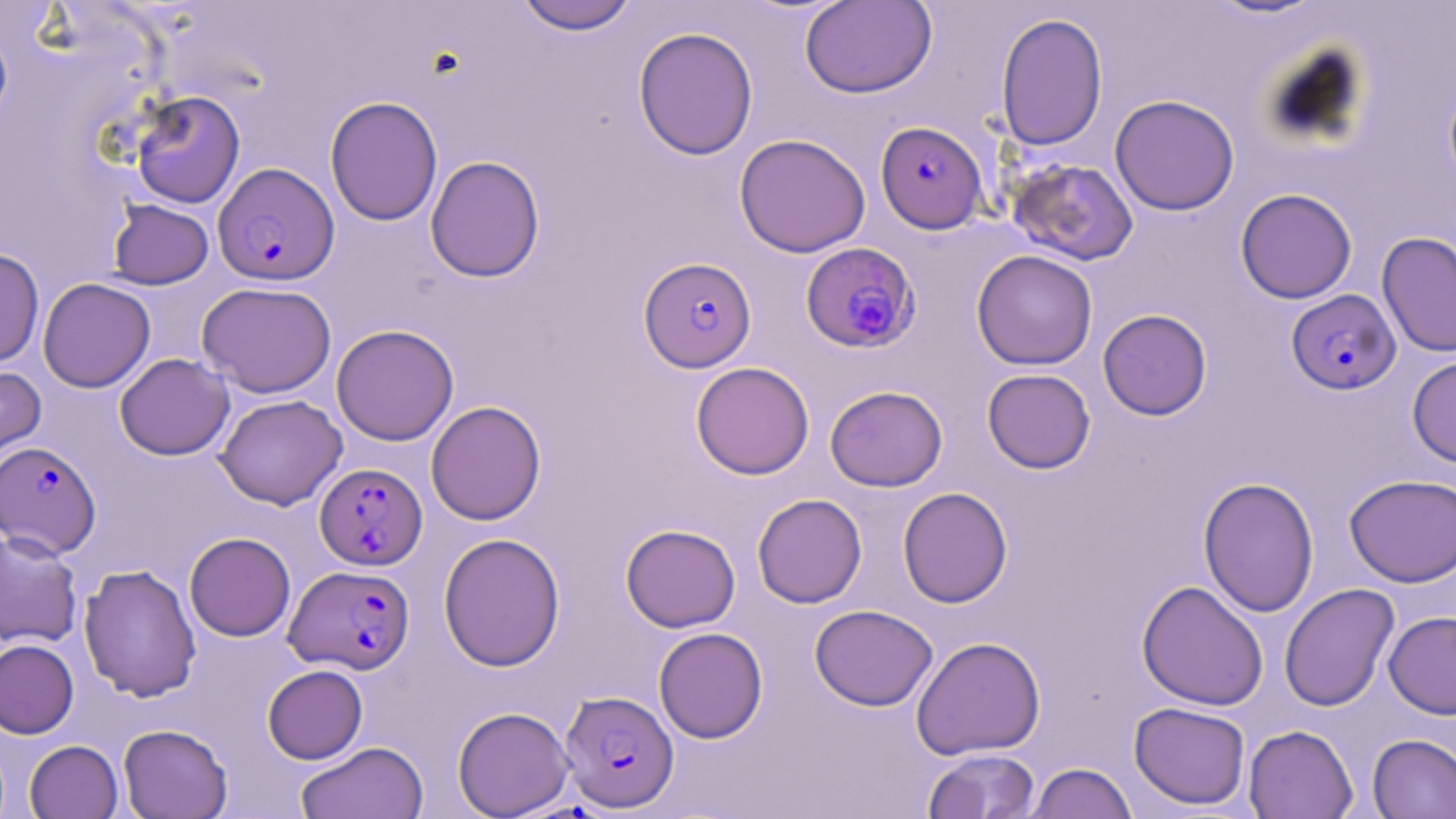
Summary:
  - Coordinate format: approximate bounding boxes as (x1, y1, x2, y2) in pixels
  - Plasmodium falciparum-infected red blood cell locations: (883, 123, 995, 242), (214, 165, 340, 288), (800, 241, 920, 352), (645, 266, 760, 373), (1286, 288, 1400, 394), (0, 441, 101, 558), (315, 462, 427, 570), (285, 565, 414, 674), (559, 689, 679, 812)
  - Uninfected red blood cell locations: (1202, 0, 1332, 21), (513, 1, 639, 35), (800, 1, 937, 98), (995, 12, 1108, 151), (0, 18, 13, 136), (633, 26, 759, 160), (1442, 71, 1456, 198), (129, 90, 245, 208), (1110, 94, 1240, 216), (325, 95, 443, 226), (734, 133, 871, 257), (425, 155, 545, 282), (1006, 158, 1139, 266), (1235, 188, 1357, 304), (107, 199, 214, 290), (1377, 232, 1456, 358), (0, 247, 44, 367), (971, 250, 1098, 370), (38, 277, 156, 393), (196, 281, 338, 398), (1098, 309, 1212, 420), (331, 324, 459, 445), (115, 353, 234, 460), (1407, 355, 1456, 468), (691, 361, 815, 479), (0, 362, 46, 478), (982, 368, 1096, 474), (825, 385, 948, 491), (215, 394, 347, 510), (425, 400, 546, 525), (1345, 473, 1456, 587), (1198, 476, 1320, 617), (897, 487, 1013, 608), (752, 493, 867, 608), (621, 524, 740, 632), (0, 529, 83, 649), (184, 532, 295, 642), (438, 532, 566, 672), (79, 563, 201, 702), (1136, 580, 1268, 710), (1279, 583, 1399, 712), (810, 604, 937, 711), (1383, 611, 1456, 719), (654, 627, 768, 743), (911, 636, 1046, 760), (0, 638, 79, 738), (262, 664, 367, 764), (1129, 701, 1250, 810), (452, 706, 575, 817), (118, 723, 233, 818), (1243, 724, 1358, 819), (1367, 733, 1456, 818), (25, 740, 123, 818), (295, 741, 429, 819), (922, 748, 1041, 819), (1026, 762, 1138, 819)
  - Slide-level diagnosis: Plasmodium falciparum
  - Preparation: thin blood smear
  - Magnification: 1000x
  - Field of view: single
  - Image size: 1456×819 pixels
  - Stain: May-Grünwald-Giemsa
  - Modality: optical microscopy